Point out each Plasmodium parasite.
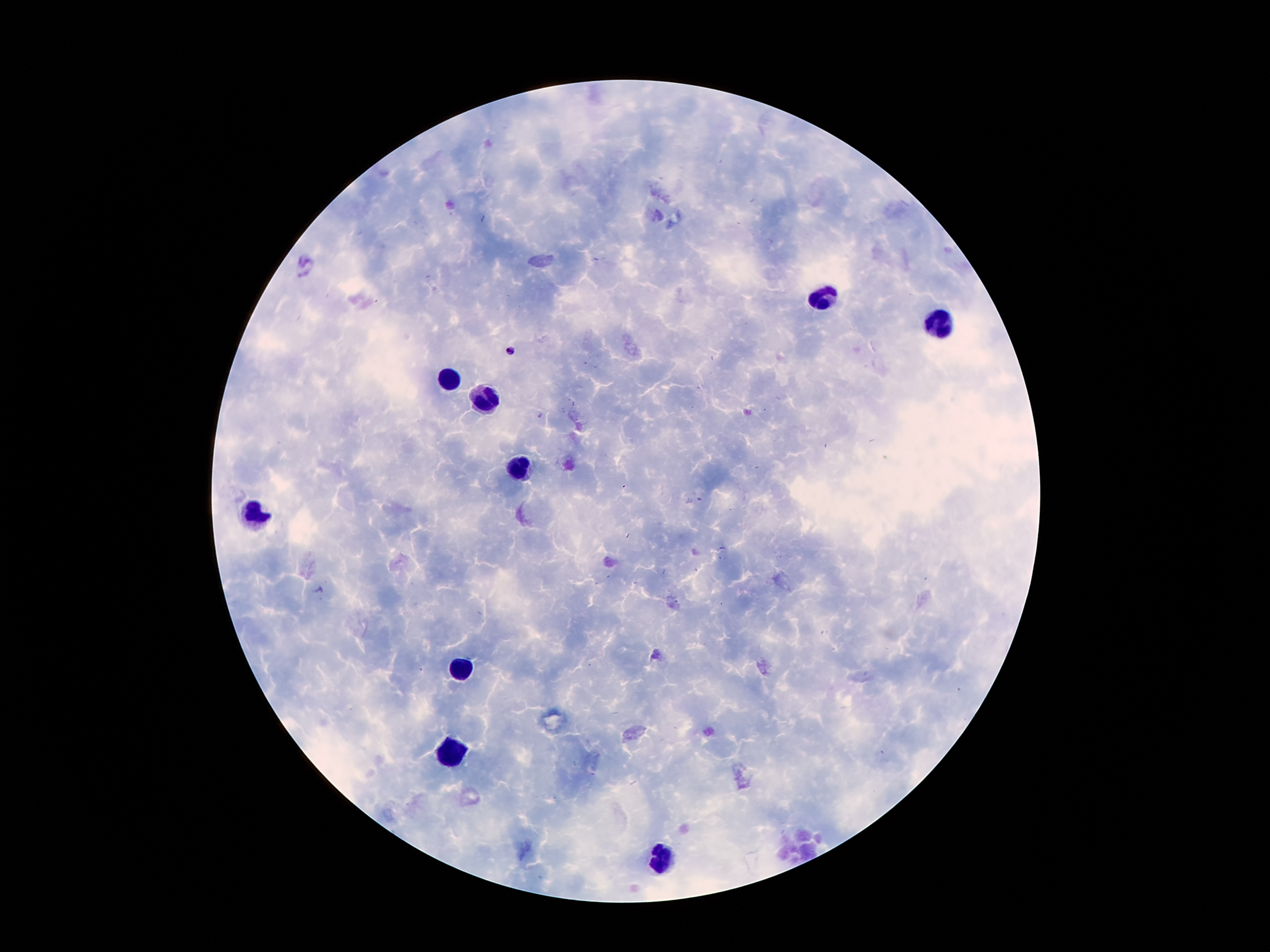

Approximate centers as {x, y} in pixels.
Plasmodium parasites: {510, 350}, {540, 416}, {699, 500}.

{
  "leukocyte_locations": "approximate centers as {x, y} in pixels: {824, 298}, {938, 325}, {445, 380}, {484, 398}, {518, 467}, {251, 513}, {459, 670}, {453, 749}, {659, 855}",
  "magnification": "100x",
  "capture": "smartphone camera through the microscope eyepiece",
  "field_of_view": "single",
  "preparation": "thick blood film",
  "stain": "Giemsa",
  "patient_malaria_status": "positive for Plasmodium falciparum",
  "image_size": "1270×952 pixels"
}